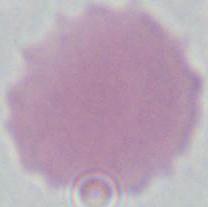

Summary:
  - Modality: photomicrograph
  - Magnification: 1000x
  - Identification: erythrocyte